Describe the morphology of the red blood cells.
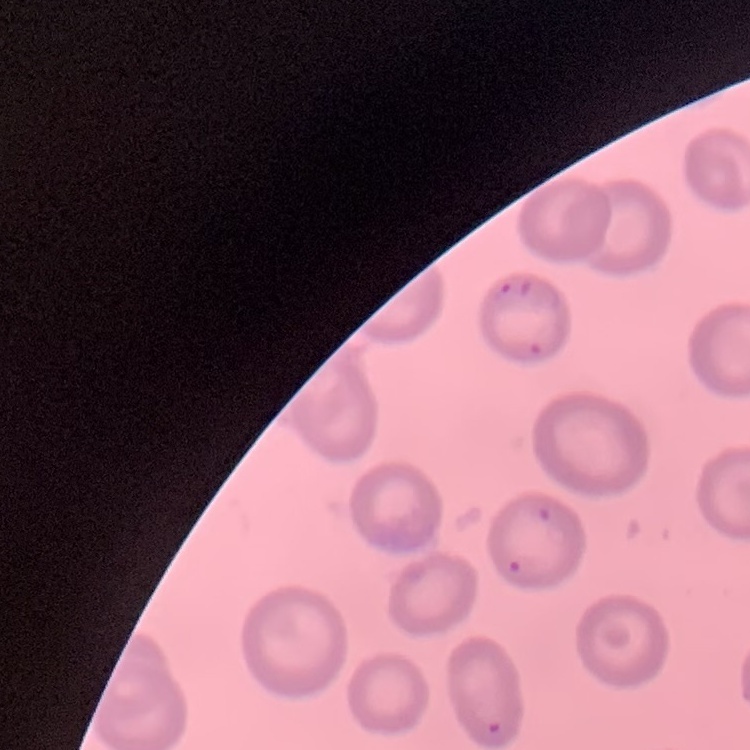

No rouleaux formation.

stain = Field's or Giemsa
image type = one tile cut from a larger photomicrograph
preparation = thin blood film